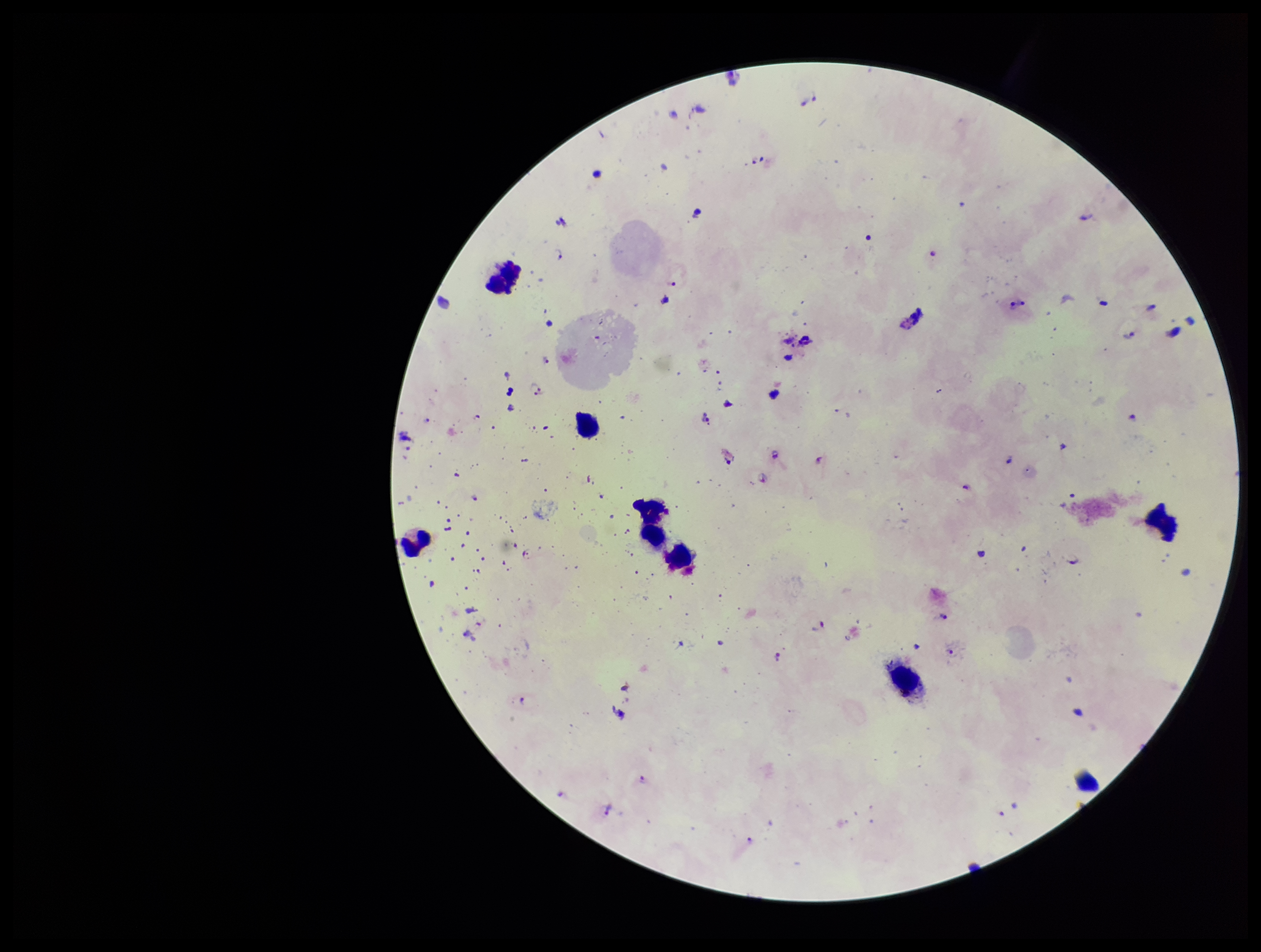
preparation = thick
stain = Giemsa
species reported for this patient = Plasmodium falciparum
parasite count = 30
image size = 1261×952 pixels
patient malaria status = positive
capture = smartphone photograph through the microscope eyepiece
leukocyte count = 7
Plasmodium parasites = identified
field of view = one from this slide